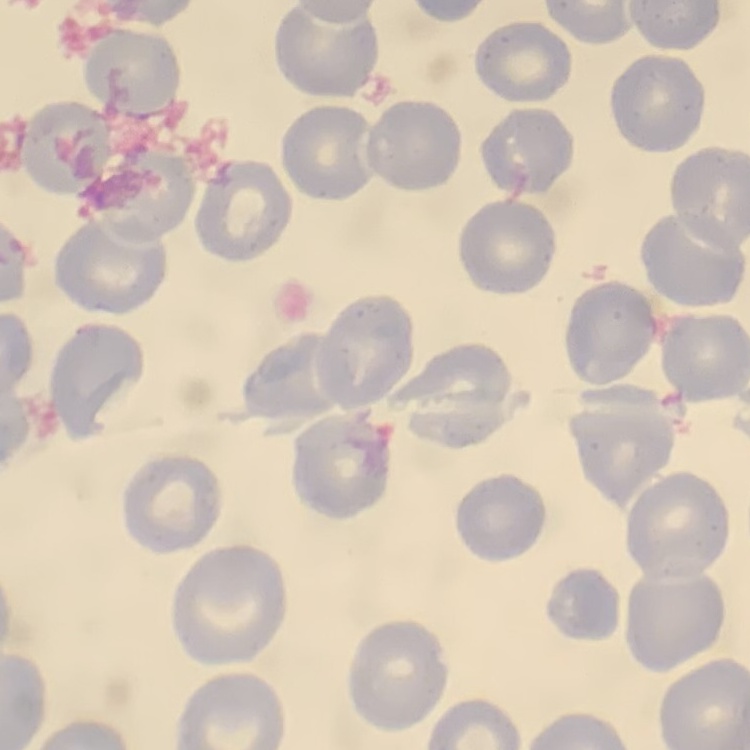
red_blood_cell_morphology: no rouleaux formation
image_type: square crop of a larger photomicrograph
preparation: thin blood smear
stain: Field's or Giemsa